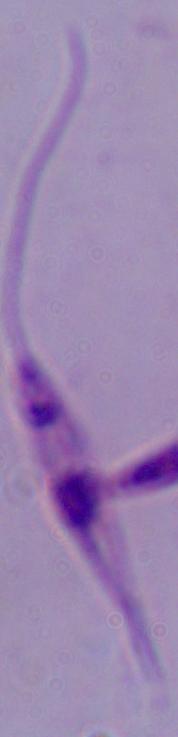

Summary:
  - Modality: photomicrograph
  - Magnification: 1000x
  - Identification: Leishmania